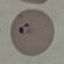
Summary:
  - Malaria status: parasitized
  - Preparation: thin smear
  - Capture: smartphone camera at the microscope eyepiece
  - Stain: Giemsa
  - Image type: cell patch, automatically extracted from a larger field of view and resized to 64 × 64 pixels